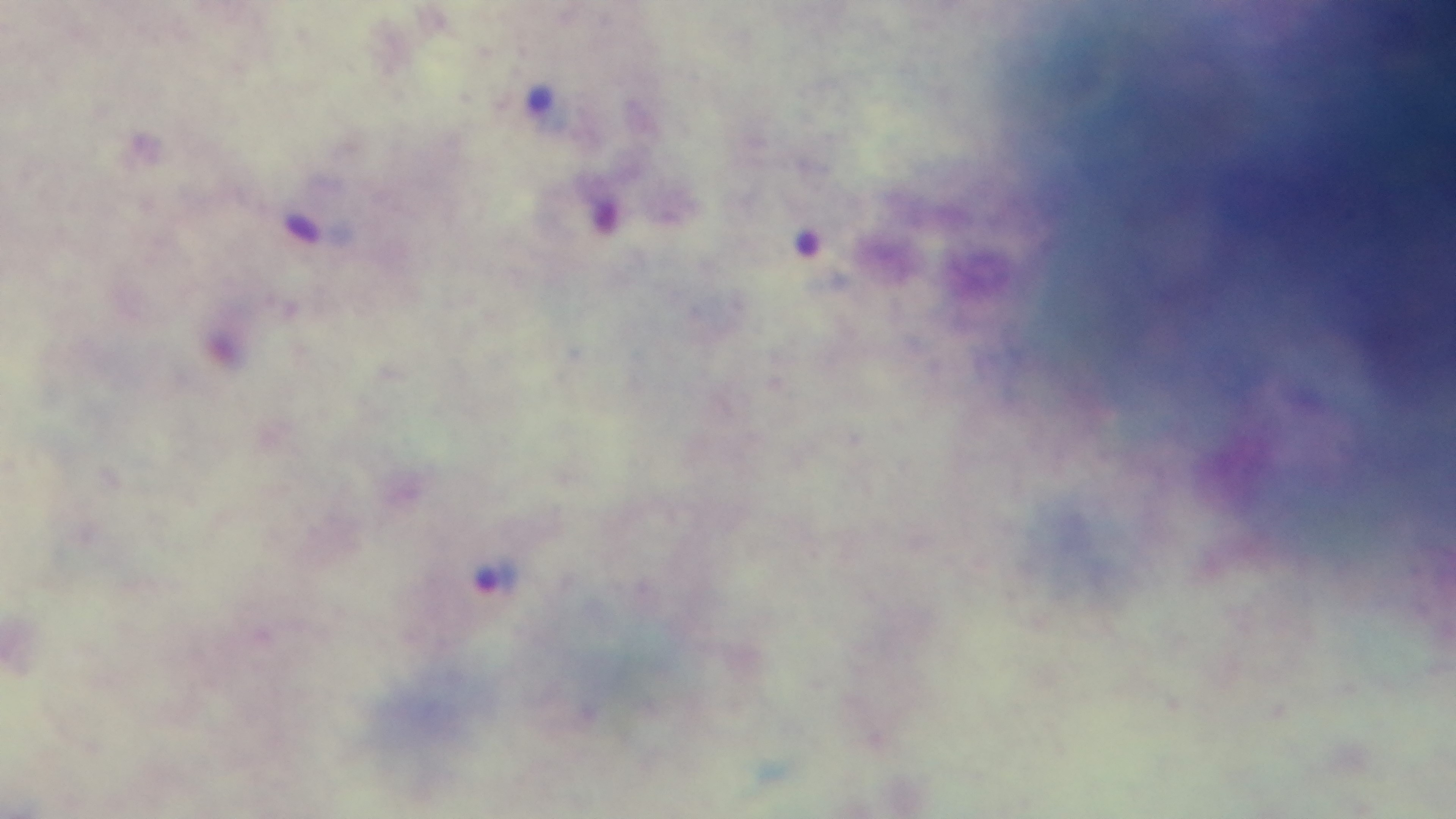
Summary:
  - Modality: light microscopy
  - Malaria status: positive
  - Capture: mounted 4K digital camera
  - Field of view: one from the slide
  - Objective: 100x oil immersion
  - Stain: Giemsa
  - Preparation: thick